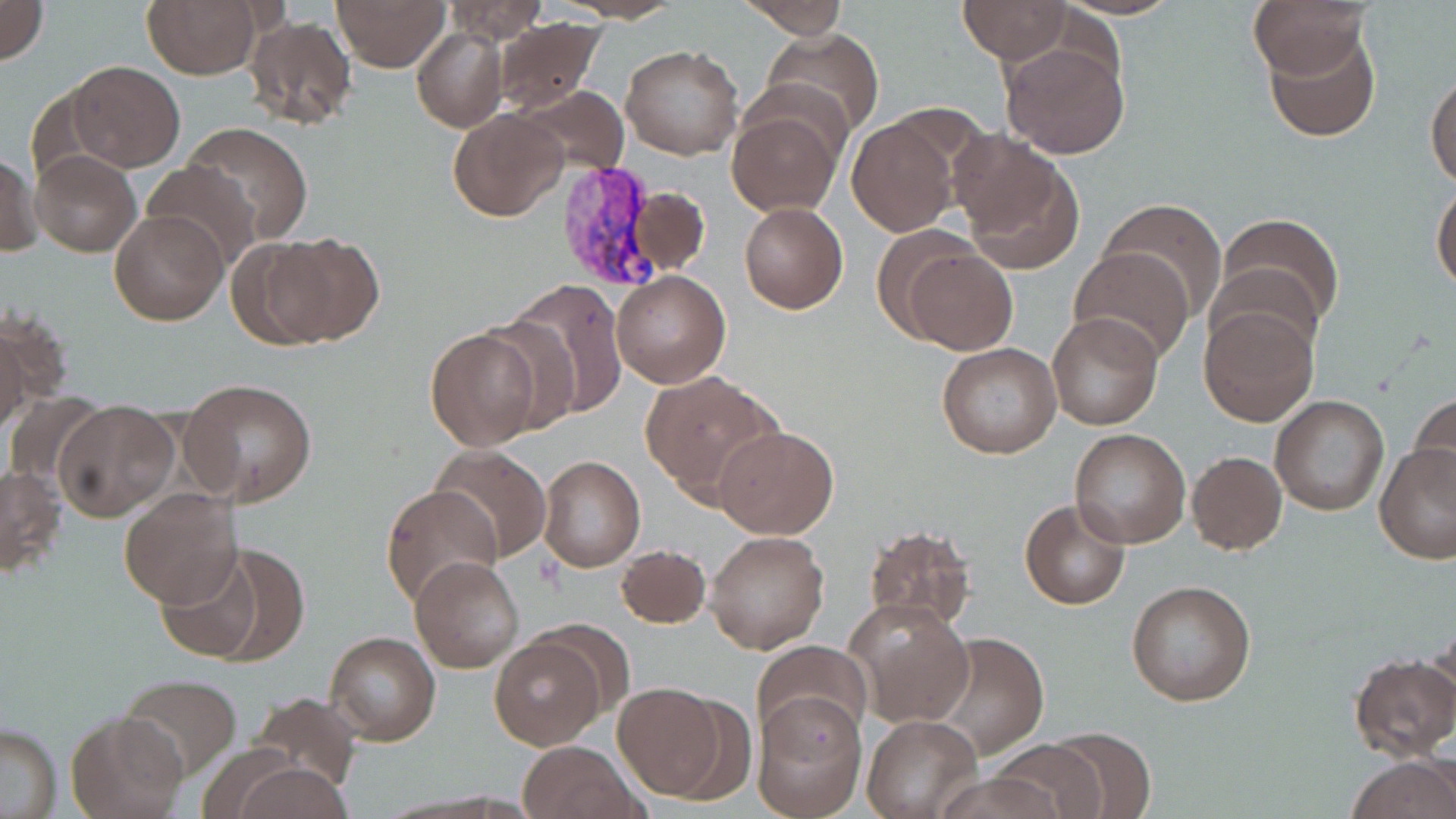

Approximate bounding boxes as (x1,y1)-(x2,y2) corner pairs in pixels. Platelet locations: (535,553)-(563,594). Uninfected red blood cell locations: (0,0)-(48,64), (142,0)-(263,78), (331,0)-(450,71), (742,0)-(851,37), (1247,0)-(1372,79), (440,1)-(547,44), (959,1)-(1071,62), (243,15)-(358,131), (491,16)-(606,116), (1263,23)-(1381,142), (412,27)-(507,132), (761,28)-(885,140), (999,34)-(1130,158), (621,44)-(744,161), (66,61)-(185,172), (1425,70)-(1456,187), (516,84)-(629,179), (446,107)-(569,223), (726,107)-(841,216), (847,116)-(963,237), (185,122)-(314,244), (954,137)-(1085,273), (0,148)-(43,258), (29,148)-(140,257), (142,160)-(258,270), (1430,181)-(1456,292), (624,185)-(709,277), (1100,197)-(1227,319), (739,202)-(847,314), (109,209)-(228,326), (1217,212)-(1344,332), (255,232)-(383,349), (900,246)-(1017,355), (1068,248)-(1195,365), (610,272)-(730,389), (500,279)-(627,419), (1199,304)-(1319,427), (2,310)-(63,429), (1046,311)-(1162,429), (473,316)-(585,435), (0,321)-(32,440), (423,326)-(542,449), (939,330)-(1166,442), (936,343)-(1060,458), (642,372)-(785,507), (180,378)-(318,506), (3,391)-(106,496), (1409,391)-(1456,497), (1269,394)-(1390,516), (53,398)-(180,521), (713,426)-(838,539), (1068,427)-(1190,548), (1376,442)-(1455,564), (431,445)-(551,563), (1187,451)-(1286,555), (537,456)-(646,573), (0,464)-(66,578), (381,482)-(502,612), (117,488)-(241,610), (1019,499)-(1131,609), (862,523)-(976,633), (706,530)-(830,654), (614,544)-(711,629), (155,548)-(275,664), (411,557)-(524,673), (1125,579)-(1257,705), (846,598)-(973,729), (537,620)-(635,715), (1425,627)-(1456,724), (928,631)-(1049,759), (325,632)-(440,745), (489,636)-(606,750), (751,639)-(870,745), (1349,654)-(1456,763), (116,673)-(241,779), (612,683)-(734,800), (249,690)-(361,797), (753,693)-(867,819), (66,710)-(186,819), (862,714)-(980,818), (0,723)-(61,817), (1041,728)-(1158,818), (985,738)-(1110,819), (518,740)-(642,819), (1348,756)-(1456,819), (236,763)-(353,819), (934,772)-(1066,818). Plasmodium vivax-infected red blood cell locations: (552,162)-(668,294). Slide-level diagnosis: Plasmodium vivax. Captured at 1000x magnification. Image is 1456×819 pixels. May-Grünwald-Giemsa stain. Single field of view. Thin blood smear. Light microscopy.